Assess this cell for malaria.
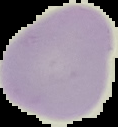
It is uninfected.

image_size: 118×127 pixels
preparation: thin blood film
image_type: segmented cell region with the area outside set to black